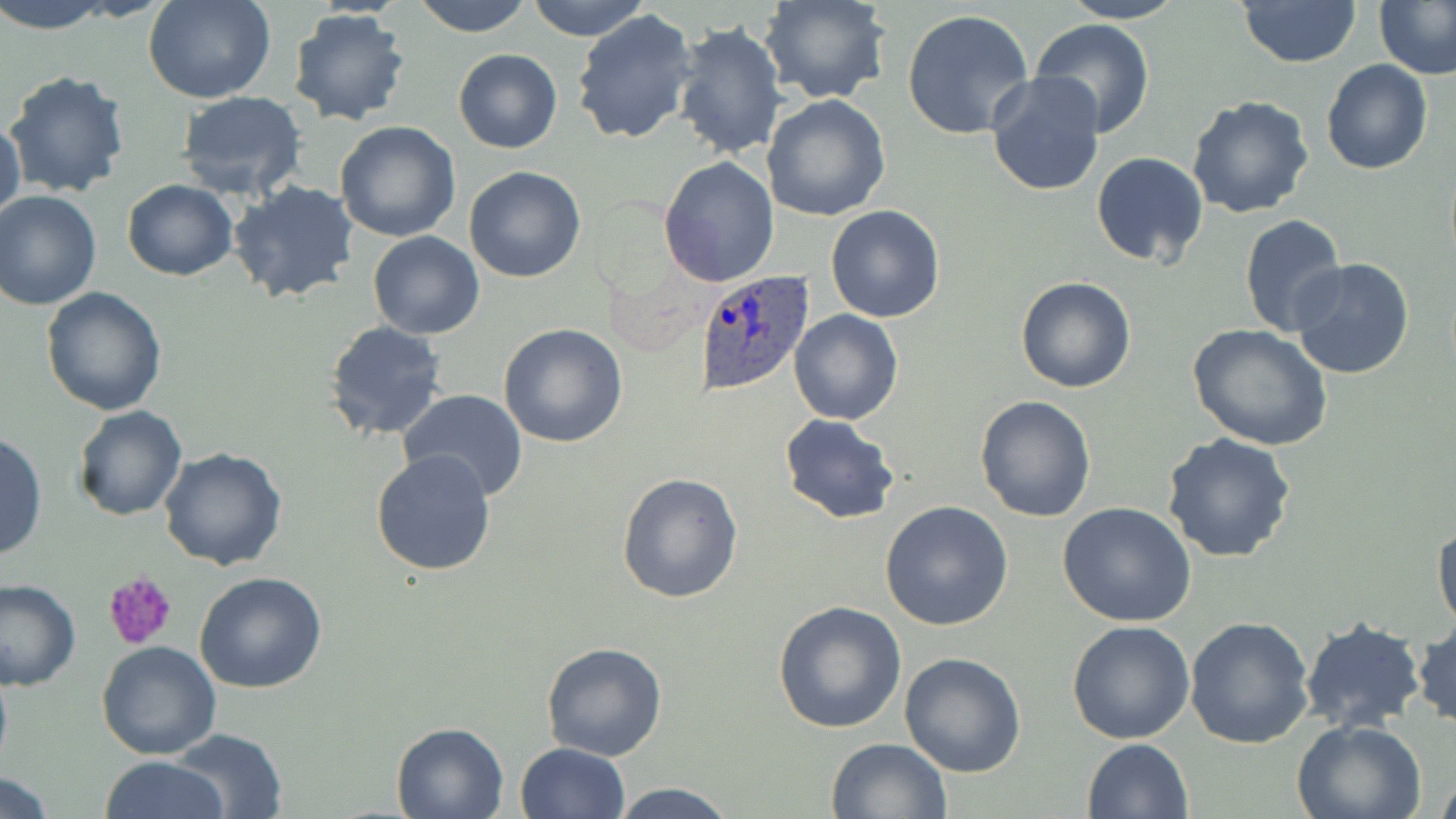 Approximate bounding boxes as (x1, y1, x2, y2) in pixels. Plasmodium ovale-infected red blood cell locations: (695, 268, 815, 393). Platelet locations: (104, 570, 177, 651). Uninfected red blood cell locations: (0, 0, 116, 34), (143, 0, 277, 104), (411, 0, 534, 37), (528, 0, 654, 41), (760, 0, 892, 105), (1059, 0, 1188, 23), (1376, 0, 1455, 81), (1237, 1, 1360, 68), (288, 8, 413, 127), (572, 8, 700, 145), (903, 8, 1035, 142), (1031, 18, 1156, 138), (672, 20, 788, 160), (453, 49, 561, 153), (1321, 58, 1433, 175), (5, 68, 131, 198), (986, 72, 1107, 195), (175, 90, 307, 201), (761, 94, 891, 223), (1187, 95, 1315, 219), (1, 114, 25, 224), (333, 121, 461, 243), (1091, 151, 1208, 269), (658, 155, 780, 286), (464, 165, 586, 283), (228, 179, 361, 305), (122, 180, 238, 281), (0, 191, 101, 311), (824, 205, 946, 324), (1238, 214, 1350, 339), (368, 232, 484, 340), (1290, 256, 1417, 380), (1015, 276, 1136, 393), (41, 285, 168, 414), (789, 310, 902, 425), (324, 320, 449, 441), (499, 323, 628, 448), (1188, 323, 1333, 450), (398, 389, 528, 502), (974, 394, 1097, 522), (72, 405, 188, 522), (779, 414, 902, 525), (1, 430, 45, 563), (1160, 431, 1296, 562), (159, 446, 288, 570), (369, 448, 497, 577), (617, 472, 745, 606), (880, 501, 1013, 630), (1058, 503, 1197, 627), (1431, 518, 1455, 636), (194, 572, 328, 695), (0, 579, 80, 690), (772, 600, 907, 735), (1298, 614, 1428, 737), (1185, 615, 1314, 750), (1066, 620, 1195, 744), (1411, 621, 1455, 728), (95, 641, 220, 760), (541, 642, 668, 761), (899, 651, 1028, 776), (1292, 718, 1428, 819), (390, 720, 512, 818), (171, 728, 287, 817), (827, 738, 951, 819), (1082, 738, 1195, 819), (515, 742, 629, 819), (102, 755, 228, 819), (1436, 770, 1456, 819), (2, 774, 56, 818), (607, 780, 742, 819). Slide-level diagnosis: Plasmodium ovale. May-Grünwald-Giemsa stain. Image is 1456×819 pixels. 1000x magnification. Single field of view. Thin blood film. Optical microscopy.